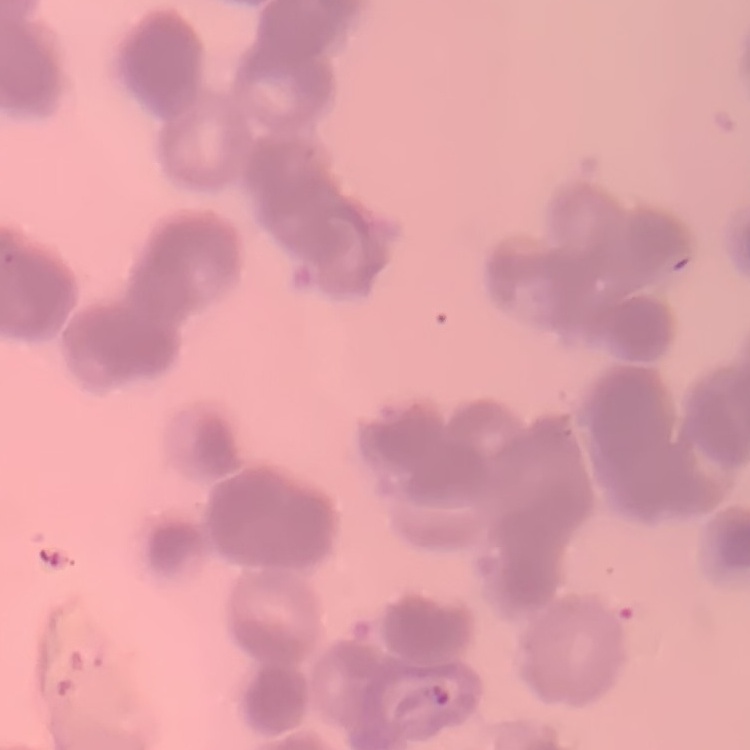
Summary:
  - Erythrocyte morphology: rouleaux formation
  - Preparation: thin blood smear
  - Image type: one tile cut from a larger photomicrograph
  - Stain: Field's or Giemsa